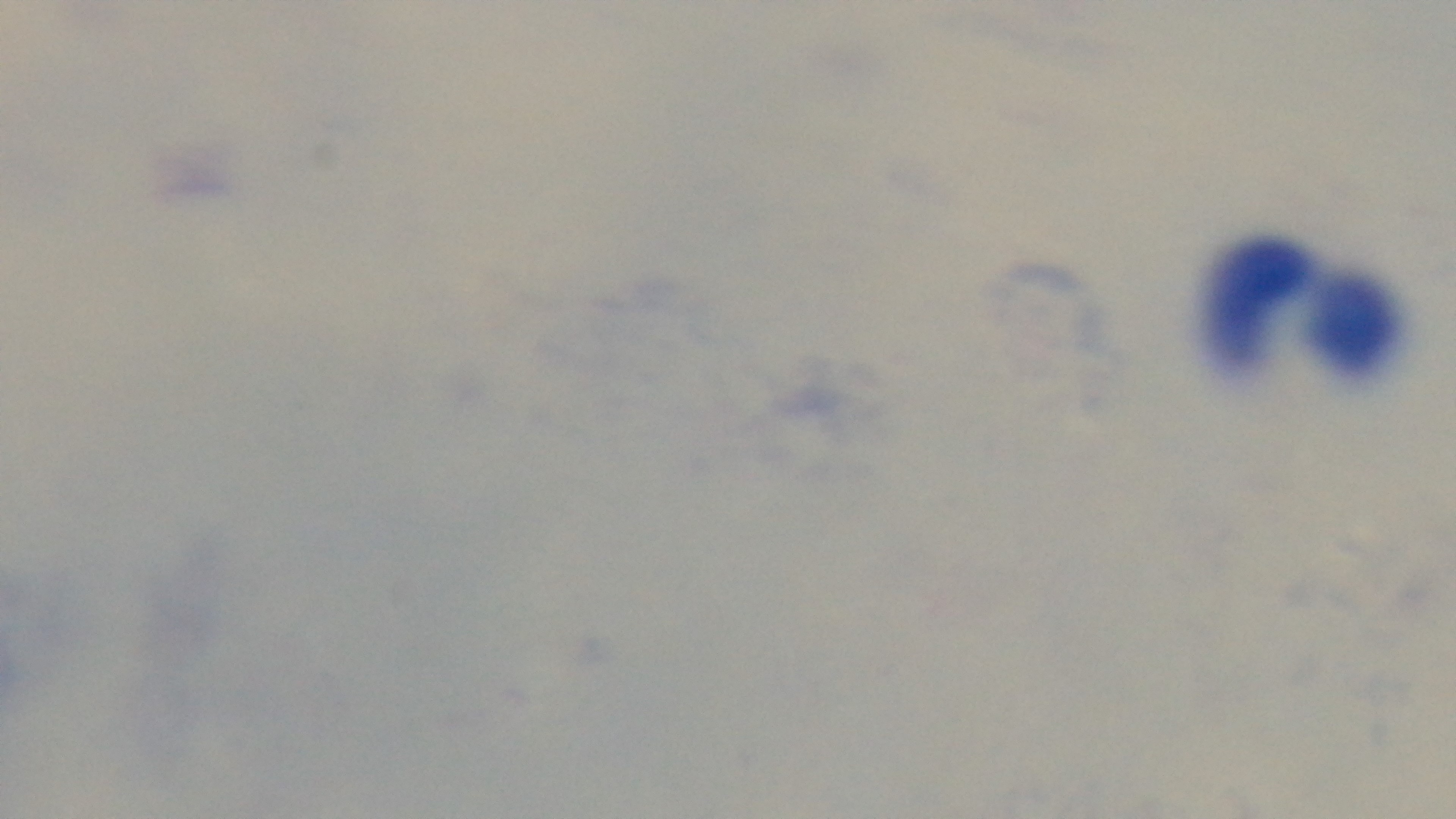

Malaria status: uninfected. One field from the slide. Preparation: thick. Light microscopy. Mounted 4K digital camera. Giemsa stain. 100x oil-immersion objective.